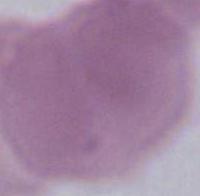

Summary:
  - Modality: micrograph
  - Magnification: 1000x
  - Identification: erythrocyte